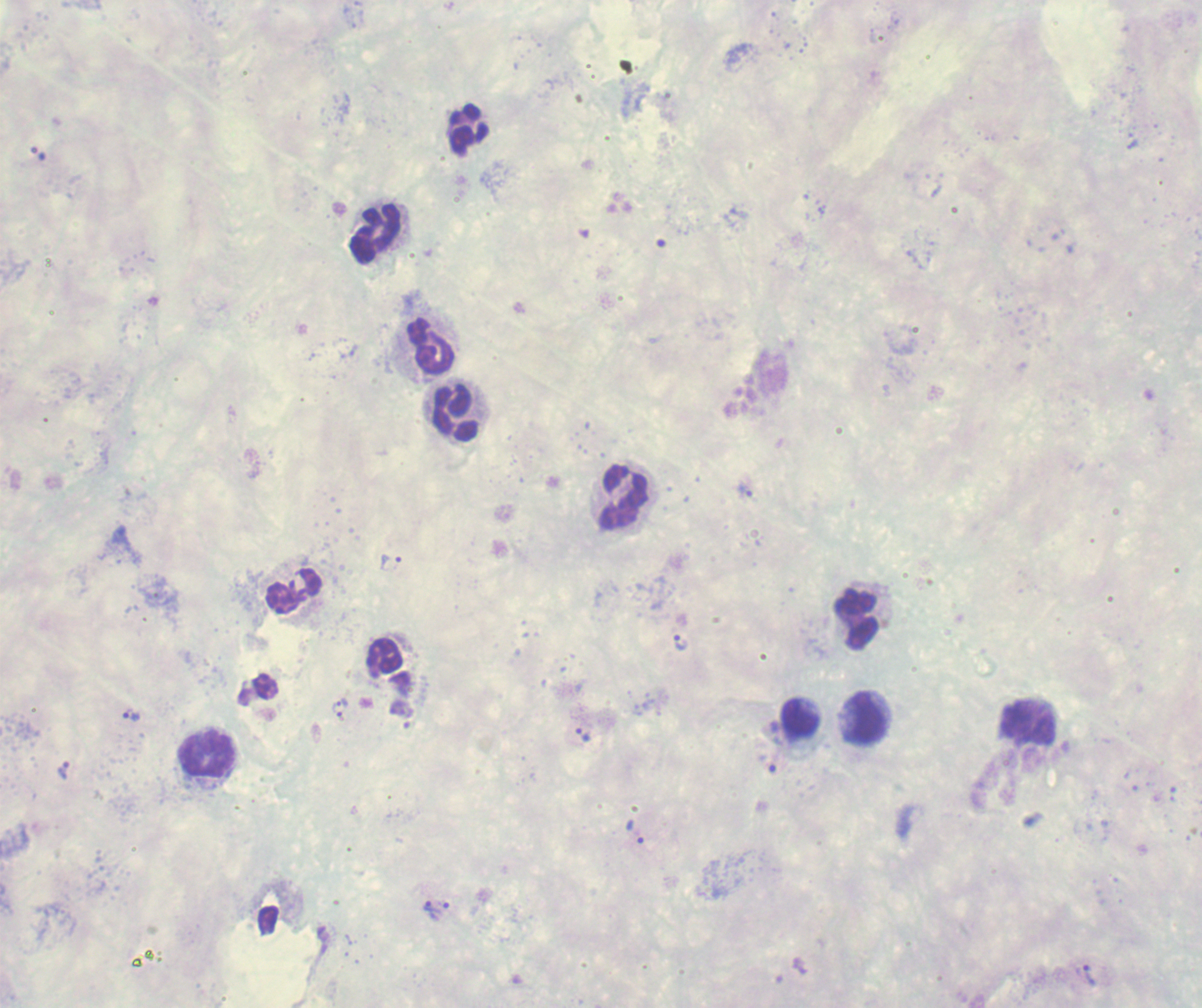
Approximate object centers, in pixels from the top-left corner. Leukocyte locations: (x=467, y=125), (x=376, y=232), (x=428, y=344), (x=457, y=413), (x=620, y=498), (x=295, y=594), (x=858, y=619), (x=385, y=657), (x=864, y=718), (x=798, y=719), (x=1030, y=723), (x=206, y=754). Trophozoite locations: (x=744, y=491), (x=391, y=562), (x=681, y=642), (x=341, y=702), (x=401, y=709), (x=132, y=716), (x=339, y=716), (x=584, y=735), (x=767, y=763), (x=64, y=771), (x=636, y=831), (x=431, y=905), (x=442, y=913). Captured at 100x magnification. Result: malaria parasites identified. Romanowsky-stained preparation. Thick blood smear. Image is 1202×1008 pixels. Previously used in an actual diagnosis. Background quality: unsatisfactory. Single field of view.